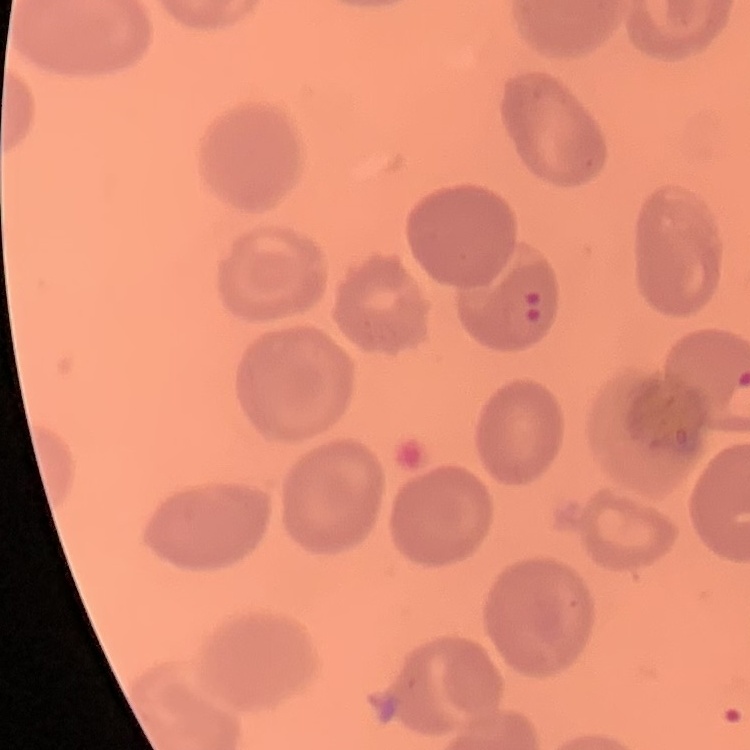
Summary:
  - Red blood cell morphology: no rouleaux formation
  - Stain: Field's or Giemsa
  - Preparation: thin blood smear
  - Image type: square crop of a larger photomicrograph